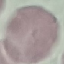

{
  "malaria_status": "uninfected",
  "stain": "Giemsa",
  "image_type": "automatically extracted cell patch, resized to 64 × 64 pixels",
  "preparation": "thin blood smear",
  "capture": "smartphone camera at the microscope eyepiece"
}